Report the malaria status of this cell.
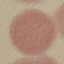
Uninfected.

capture = smartphone camera at the microscope eyepiece
stain = Giemsa
image type = cell patch, automatically extracted from a larger field of view and resized to 64 × 64 pixels
preparation = thin blood film